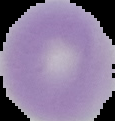
Result: negative for Plasmodium parasites. From a thin blood film. Image is 115×121 pixels. Cell region segmented out of the field of view; the surrounding area is masked to black.